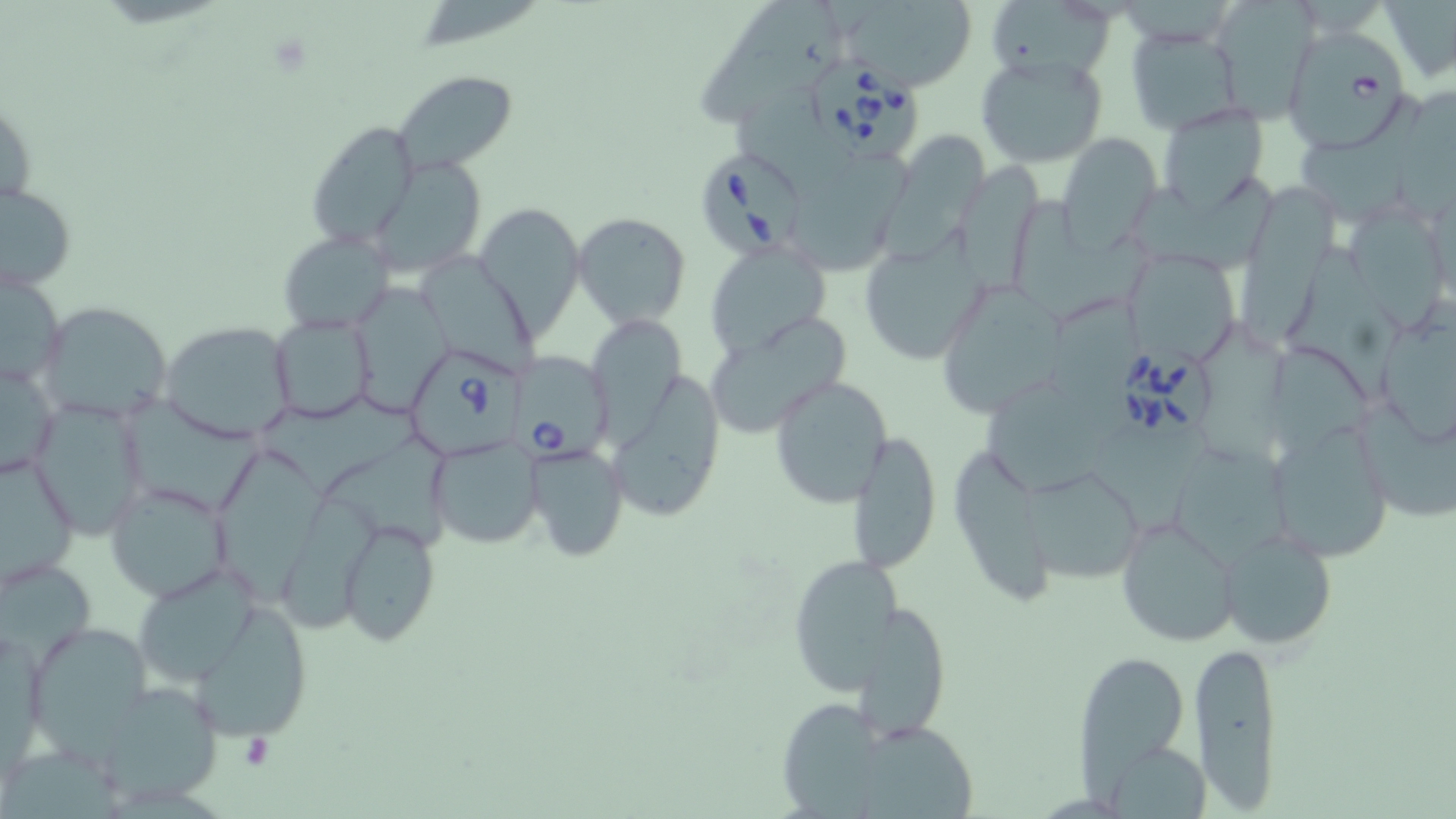
{
  "babesia_divergens_infected_red_blood_cell_locations": "approximate bounding boxes as named x1/y1/x2/y2 corners in pixels: (x1=1291, y1=31, x2=1407, y2=152), (x1=811, y1=56, x2=922, y2=162), (x1=700, y1=145, x2=804, y2=254), (x1=1115, y1=344, x2=1214, y2=439), (x1=407, y1=347, x2=526, y2=465), (x1=507, y1=354, x2=618, y2=462)",
  "slide_level_diagnosis": "Babesia divergens",
  "magnification": "1000x",
  "stain": "May-Grünwald-Giemsa",
  "field_of_view": "one of a larger specimen",
  "platelet_locations": "approximate bounding boxes as named x1/y1/x2/y2 corners in pixels: (x1=241, y1=734, x2=274, y2=771)",
  "modality": "light microscopy",
  "image_size": "1456×819 pixels",
  "preparation": "thin blood film",
  "uninfected_red_blood_cell_locations": "approximate bounding boxes as named x1/y1/x2/y2 corners in pixels: (x1=833, y1=1, x2=977, y2=89), (x1=699, y1=4, x2=835, y2=131), (x1=1124, y1=26, x2=1244, y2=133), (x1=976, y1=51, x2=1109, y2=169), (x1=393, y1=69, x2=517, y2=177), (x1=732, y1=77, x2=842, y2=184), (x1=1155, y1=103, x2=1270, y2=211), (x1=307, y1=119, x2=418, y2=250), (x1=1057, y1=132, x2=1160, y2=251), (x1=370, y1=157, x2=489, y2=274), (x1=791, y1=172, x2=913, y2=274), (x1=877, y1=172, x2=978, y2=262), (x1=961, y1=174, x2=1044, y2=295), (x1=1132, y1=177, x2=1282, y2=269), (x1=1236, y1=180, x2=1334, y2=350), (x1=1, y1=181, x2=77, y2=293), (x1=1016, y1=200, x2=1149, y2=321), (x1=476, y1=204, x2=586, y2=340), (x1=572, y1=211, x2=691, y2=329), (x1=1349, y1=215, x2=1445, y2=336), (x1=278, y1=231, x2=394, y2=335), (x1=858, y1=236, x2=987, y2=366), (x1=706, y1=241, x2=832, y2=356), (x1=1280, y1=245, x2=1402, y2=404), (x1=416, y1=246, x2=536, y2=375), (x1=1129, y1=254, x2=1239, y2=364), (x1=0, y1=265, x2=66, y2=389), (x1=354, y1=277, x2=456, y2=418), (x1=942, y1=283, x2=1067, y2=413), (x1=1046, y1=293, x2=1143, y2=397), (x1=36, y1=300, x2=175, y2=427), (x1=1369, y1=304, x2=1456, y2=451), (x1=268, y1=313, x2=378, y2=425), (x1=594, y1=314, x2=689, y2=452), (x1=703, y1=316, x2=853, y2=441), (x1=158, y1=319, x2=299, y2=444), (x1=1253, y1=343, x2=1377, y2=450), (x1=0, y1=354, x2=61, y2=483), (x1=605, y1=363, x2=727, y2=526), (x1=767, y1=374, x2=893, y2=507), (x1=987, y1=381, x2=1110, y2=491), (x1=29, y1=396, x2=151, y2=543), (x1=133, y1=397, x2=269, y2=508), (x1=262, y1=397, x2=423, y2=497), (x1=1355, y1=397, x2=1456, y2=525), (x1=1265, y1=418, x2=1398, y2=564), (x1=1083, y1=426, x2=1210, y2=532), (x1=847, y1=431, x2=941, y2=574), (x1=328, y1=434, x2=456, y2=551), (x1=427, y1=436, x2=543, y2=550), (x1=525, y1=442, x2=628, y2=562), (x1=953, y1=443, x2=1051, y2=611), (x1=214, y1=447, x2=325, y2=605), (x1=1175, y1=448, x2=1292, y2=571), (x1=0, y1=450, x2=77, y2=590), (x1=1024, y1=468, x2=1142, y2=583), (x1=104, y1=480, x2=237, y2=603), (x1=282, y1=491, x2=378, y2=639), (x1=337, y1=516, x2=442, y2=643), (x1=1117, y1=516, x2=1241, y2=648), (x1=1219, y1=527, x2=1337, y2=651), (x1=788, y1=552, x2=908, y2=688), (x1=1, y1=555, x2=96, y2=664), (x1=131, y1=564, x2=263, y2=686), (x1=185, y1=599, x2=315, y2=744), (x1=849, y1=605, x2=956, y2=742), (x1=26, y1=620, x2=155, y2=755), (x1=1, y1=624, x2=46, y2=773), (x1=1189, y1=638, x2=1285, y2=812), (x1=1075, y1=648, x2=1193, y2=785), (x1=90, y1=682, x2=227, y2=806), (x1=776, y1=699, x2=890, y2=819), (x1=860, y1=723, x2=980, y2=817), (x1=1100, y1=739, x2=1210, y2=817)"
}